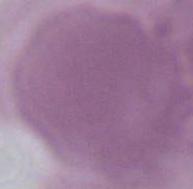

{
  "modality": "photomicrograph",
  "magnification": "1000x",
  "identification": "erythrocyte"
}